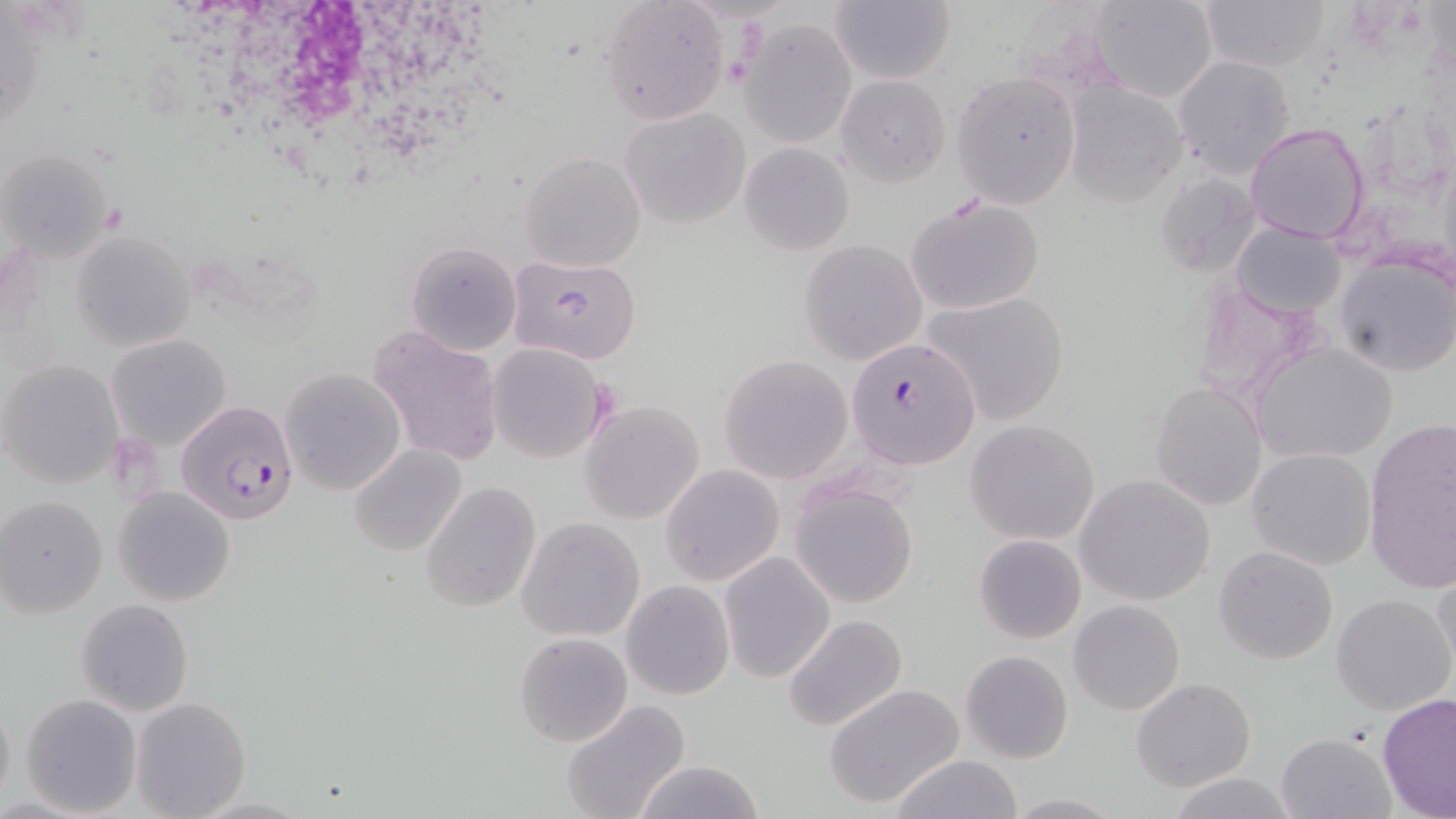

slide-level diagnosis = Plasmodium falciparum
modality = light microscopy
uninfected red blood cell locations = approximate bounding boxes as (x1,y1)-(x2,y2) corner pairs in pixels: (1087,0)-(1219,102), (1198,0)-(1328,73), (828,1)-(955,85), (598,2)-(729,125), (739,16)-(857,147), (1172,54)-(1295,179), (950,71)-(1081,208), (836,74)-(951,188), (1063,83)-(1188,206), (619,106)-(750,227), (1246,122)-(1367,245), (738,142)-(855,255), (1,146)-(117,266), (520,152)-(646,272), (1154,173)-(1264,280), (903,195)-(1046,316), (1230,219)-(1348,319), (70,230)-(196,350), (798,238)-(927,366), (407,240)-(523,356), (1334,248)-(1456,379), (505,254)-(643,365), (923,291)-(1069,425), (369,326)-(506,467), (105,333)-(232,452), (1254,341)-(1398,464), (487,343)-(609,464), (718,353)-(855,483), (0,359)-(123,489), (281,366)-(406,495), (1150,382)-(1269,511), (579,400)-(704,524), (965,419)-(1100,545), (1362,422)-(1454,596), (350,445)-(467,558), (1247,447)-(1376,571), (660,465)-(784,586), (1074,474)-(1215,605), (419,481)-(542,612), (789,481)-(918,609), (114,486)-(235,605), (2,495)-(106,616), (516,516)-(645,642), (974,533)-(1087,644), (1214,545)-(1339,665), (720,551)-(835,683), (1431,566)-(1456,683), (621,580)-(735,700), (1332,593)-(1453,714), (75,599)-(193,715), (1068,600)-(1185,716), (782,614)-(908,733), (513,632)-(632,747), (959,650)-(1073,764), (1132,677)-(1256,789), (824,683)-(967,808), (0,693)-(15,811), (20,693)-(142,817), (1378,693)-(1456,819), (132,697)-(250,818), (563,699)-(690,819), (1276,732)-(1394,818), (889,755)-(1026,819), (632,758)-(769,819), (1165,772)-(1299,818), (1001,793)-(1127,817)
field of view = one of a larger specimen
magnification = 1000x
platelet locations = approximate bounding boxes as (x1,y1)-(x2,y2) corner pairs in pixels: (724,58)-(751,87)
white blood cell locations = approximate bounding boxes as (x1,y1)-(x2,y2) corner pairs in pixels: (209,2)-(484,184)
Plasmodium falciparum-infected red blood cell locations = approximate bounding boxes as (x1,y1)-(x2,y2) corner pairs in pixels: (847,334)-(980,468), (177,399)-(301,526)
preparation = thin blood film
image size = 1456×819 pixels
stain = May-Grünwald-Giemsa